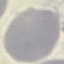
Result: no malaria parasites seen. Thin smear of blood. Automatically extracted cell patch, resized to 64 × 64 pixels. Acquired by smartphone through the microscope eyepiece. Giemsa-stained preparation.